Identify the parasite.
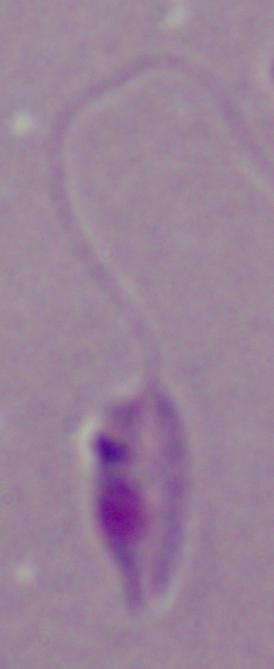

This is Leishmania.

Photomicrograph. Captured at 1000x magnification.